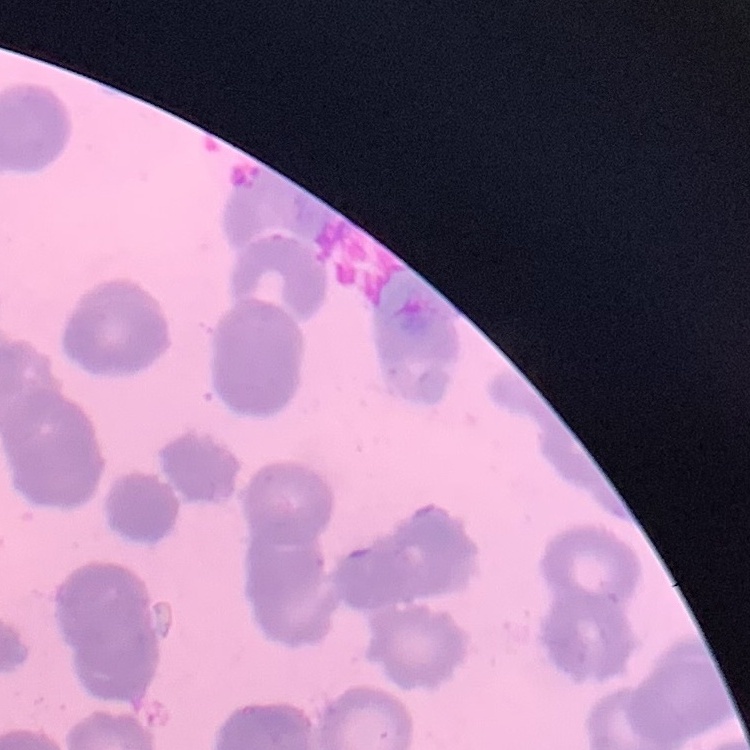
erythrocyte morphology = rouleaux formation
preparation = thin peripheral smear
image type = one tile cut from a larger photomicrograph
stain = Field's or Giemsa